Assess this cell for malaria.
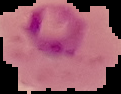
Parasitized.

Image is 121×94 pixels. From a thin blood smear. The area outside the segmented cell region is set to black.